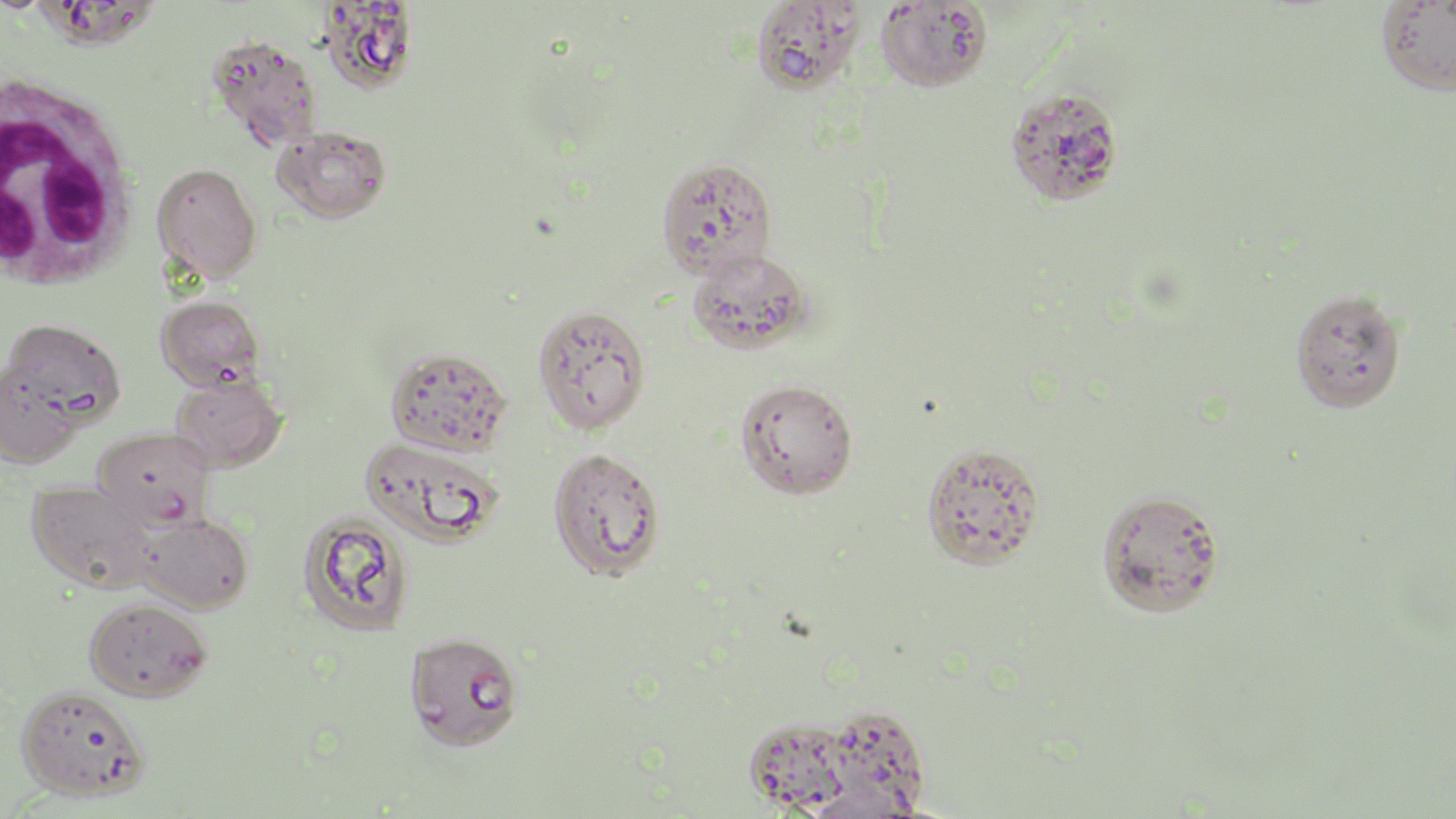

Summary:
  - Coordinate format: approximate bounding boxes as named x1/y1/x2/y2 corners in pixels
  - Uninfected red blood cell locations: (x1=40, y1=0, x2=170, y2=53), (x1=750, y1=0, x2=866, y2=96), (x1=875, y1=1, x2=992, y2=93), (x1=1375, y1=1, x2=1456, y2=96), (x1=318, y1=2, x2=420, y2=95), (x1=207, y1=34, x2=323, y2=151), (x1=1004, y1=84, x2=1126, y2=207), (x1=273, y1=125, x2=391, y2=223), (x1=655, y1=156, x2=778, y2=279), (x1=152, y1=162, x2=262, y2=282), (x1=686, y1=249, x2=814, y2=355), (x1=1289, y1=288, x2=1408, y2=414), (x1=155, y1=294, x2=265, y2=390), (x1=531, y1=303, x2=651, y2=435), (x1=2, y1=317, x2=126, y2=430), (x1=385, y1=345, x2=513, y2=456), (x1=0, y1=361, x2=83, y2=467), (x1=171, y1=374, x2=287, y2=472), (x1=734, y1=378, x2=859, y2=499), (x1=94, y1=429, x2=216, y2=530), (x1=360, y1=436, x2=503, y2=547), (x1=920, y1=442, x2=1046, y2=571), (x1=546, y1=446, x2=665, y2=581), (x1=27, y1=480, x2=155, y2=593), (x1=1095, y1=487, x2=1226, y2=618), (x1=298, y1=512, x2=413, y2=635), (x1=137, y1=513, x2=254, y2=614), (x1=83, y1=597, x2=212, y2=702), (x1=404, y1=631, x2=524, y2=750), (x1=15, y1=684, x2=150, y2=801), (x1=816, y1=706, x2=932, y2=818), (x1=742, y1=716, x2=856, y2=815)
  - White blood cell locations: (x1=0, y1=71, x2=142, y2=297)
  - Slide-level diagnosis: Plasmodium falciparum
  - Image size: 1456×819 pixels
  - Preparation: thin blood smear
  - Magnification: 1000x
  - Modality: light microscopy
  - Field of view: single
  - Stain: May-Grünwald-Giemsa